State the blood parasite species.
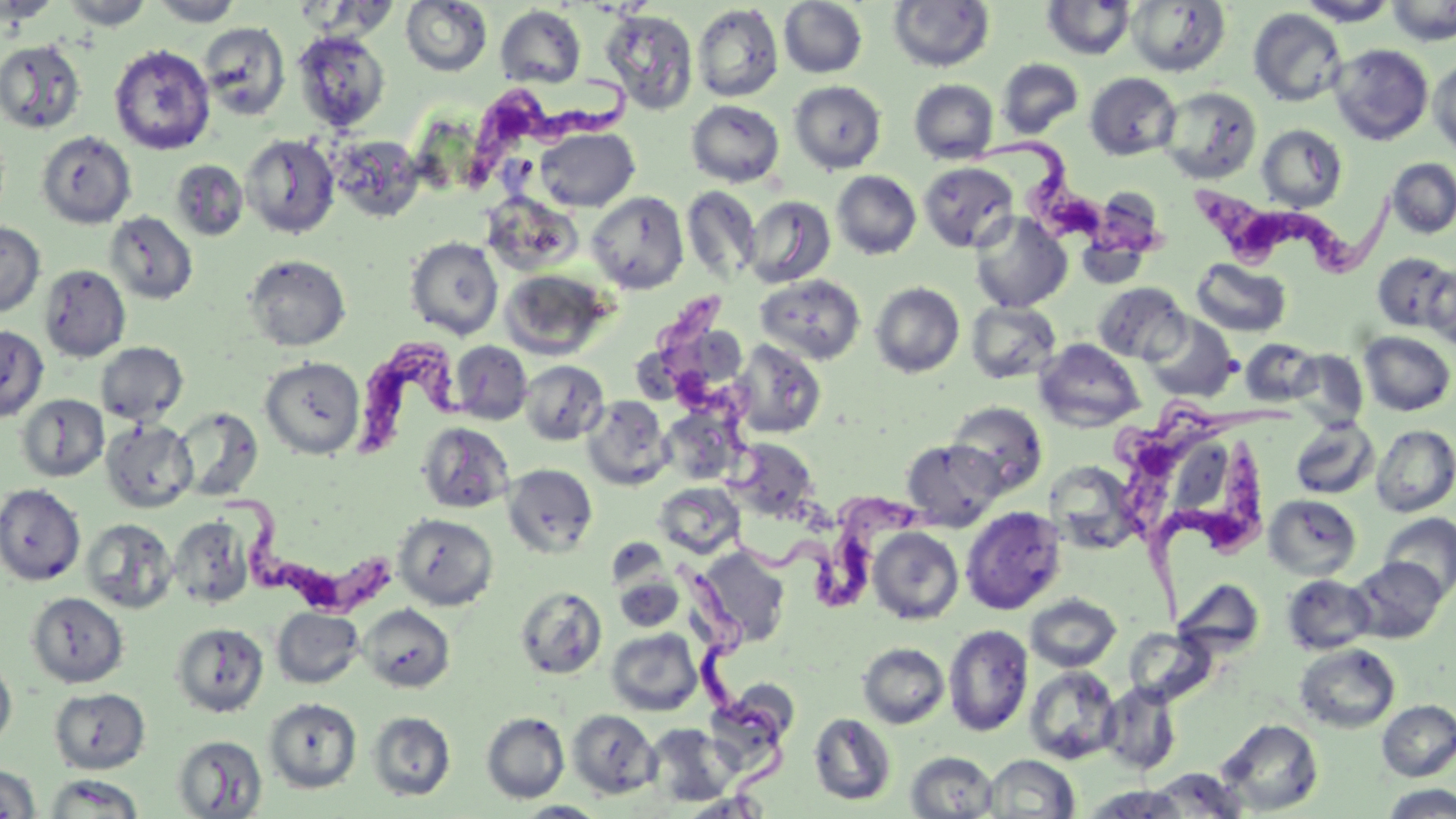

Trypanosoma brucei.

field of view = single
preparation = thin blood film
uninfected red blood cell locations = approximate bounding boxes as (x1, y1, x2, y2) in pixels: (1, 0, 58, 25), (60, 0, 154, 30), (149, 0, 245, 26), (400, 0, 492, 76), (779, 0, 868, 78), (888, 0, 995, 72), (1126, 0, 1230, 76), (1296, 0, 1399, 26), (1386, 0, 1455, 46), (1042, 1, 1136, 60), (692, 3, 784, 103), (495, 5, 586, 88), (1248, 8, 1348, 106), (600, 9, 698, 115), (199, 21, 290, 121), (292, 31, 390, 131), (0, 39, 86, 134), (109, 44, 215, 155), (1329, 44, 1434, 145), (1429, 57, 1456, 157), (997, 58, 1083, 139), (1085, 72, 1181, 160), (909, 79, 999, 164), (789, 80, 886, 174), (1158, 87, 1262, 184), (686, 99, 785, 186), (1256, 124, 1348, 211), (535, 127, 639, 212), (37, 131, 136, 229), (241, 134, 340, 238), (330, 135, 425, 222), (1386, 158, 1456, 238), (171, 159, 248, 241), (919, 162, 1018, 252), (832, 170, 921, 260), (682, 186, 761, 283), (587, 191, 689, 294), (743, 195, 835, 288), (106, 211, 198, 304), (969, 212, 1072, 312), (0, 222, 45, 317), (405, 236, 504, 340), (1372, 252, 1454, 332), (244, 254, 351, 352), (1191, 257, 1292, 337), (1423, 263, 1456, 350), (40, 264, 131, 361), (500, 269, 613, 361), (755, 273, 866, 365), (870, 281, 965, 377), (1093, 282, 1190, 364), (966, 302, 1061, 384), (1144, 313, 1239, 402), (0, 324, 48, 421), (1358, 331, 1455, 416), (1240, 338, 1320, 406), (732, 339, 826, 439), (1034, 339, 1145, 431), (451, 341, 532, 425), (95, 342, 188, 425), (1288, 350, 1369, 428), (260, 357, 364, 458), (519, 360, 608, 445), (17, 393, 109, 482), (582, 395, 673, 490), (947, 401, 1047, 496), (173, 406, 263, 500), (1289, 417, 1379, 500), (101, 418, 197, 513), (418, 421, 514, 514), (1372, 425, 1456, 517), (729, 438, 819, 521), (901, 439, 1004, 529), (1046, 461, 1139, 554), (503, 463, 598, 557), (655, 482, 745, 559), (0, 484, 85, 585), (1264, 494, 1362, 580), (961, 506, 1066, 615), (1379, 512, 1456, 600), (393, 513, 498, 610), (169, 516, 254, 609), (81, 518, 177, 613), (868, 527, 964, 624), (696, 545, 791, 648), (1348, 556, 1447, 644), (1282, 574, 1376, 655), (614, 575, 685, 632), (1173, 580, 1266, 658), (514, 586, 607, 679), (27, 591, 128, 687), (1025, 593, 1122, 672), (359, 604, 455, 693), (272, 608, 364, 688), (171, 622, 269, 717), (943, 624, 1033, 737), (1124, 627, 1215, 703), (606, 628, 703, 716), (858, 643, 949, 729), (1295, 643, 1401, 733), (0, 658, 17, 752), (1024, 665, 1121, 765), (1100, 681, 1182, 775), (49, 687, 150, 774), (263, 698, 362, 793), (1377, 699, 1456, 781), (566, 709, 660, 798), (368, 711, 455, 801), (481, 712, 570, 803), (809, 712, 896, 806), (1218, 718, 1323, 815), (645, 724, 737, 807), (172, 734, 268, 818), (906, 751, 998, 818), (982, 754, 1080, 817), (0, 764, 41, 818), (1144, 767, 1249, 817), (43, 774, 145, 817), (1379, 784, 1456, 818), (1079, 786, 1193, 818), (677, 791, 771, 818), (514, 801, 609, 818)
stain = May-Grünwald-Giemsa
image size = 1456×819 pixels
magnification = 1000x
modality = light microscopy
Trypanosoma brucei locations = approximate bounding boxes as (x1, y1, x2, y2) in pixels: (473, 68, 627, 186), (976, 140, 1181, 263), (1186, 170, 1393, 278), (653, 297, 760, 494), (350, 332, 496, 458), (1110, 395, 1308, 546), (1148, 442, 1280, 641), (216, 478, 403, 627), (719, 487, 934, 605), (665, 558, 798, 802)